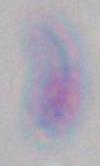 Micrograph. Toxoplasma gondii is seen. Captured at 1000x magnification.